Give the position of every Plasmodium parasite visible.
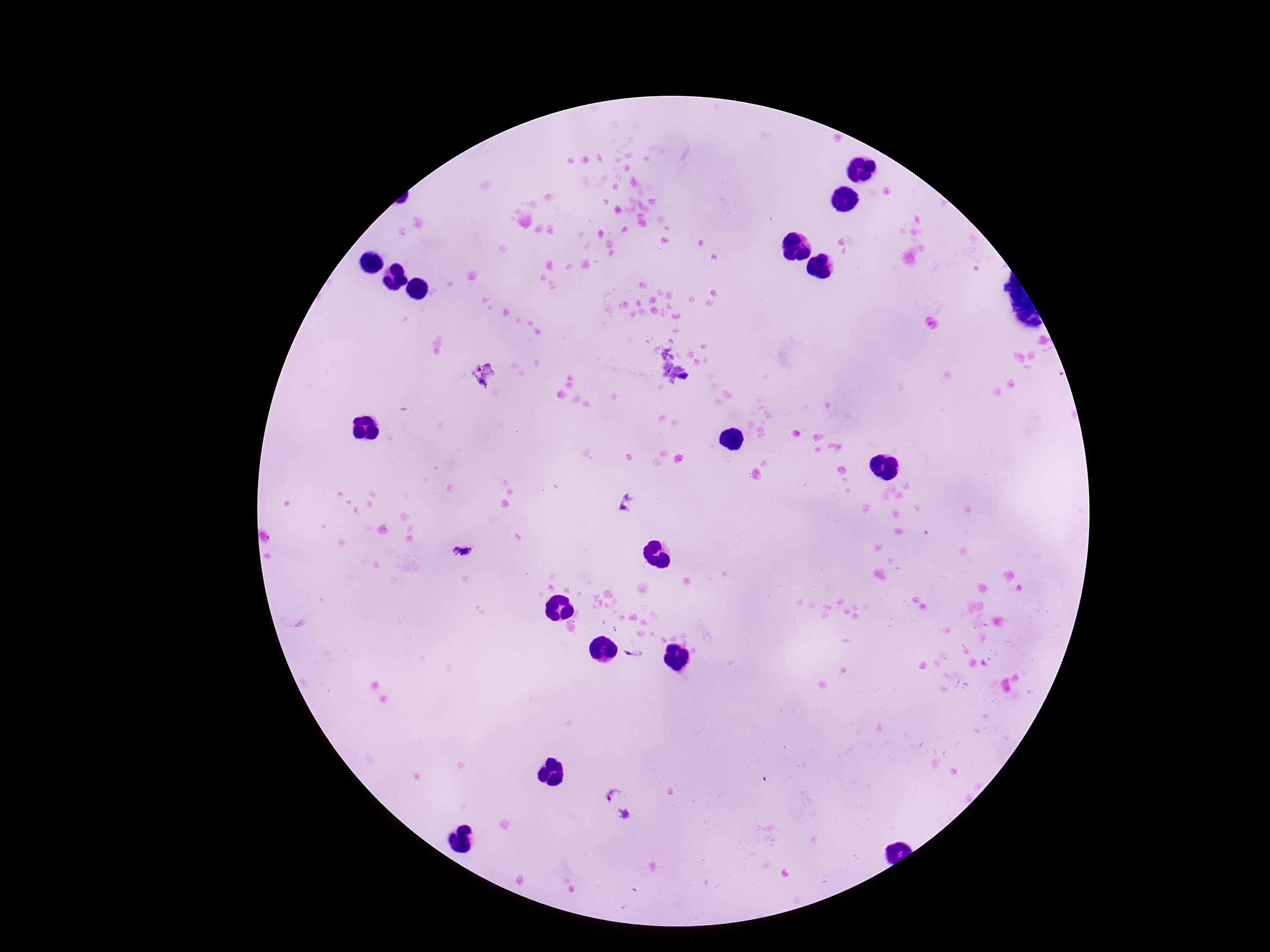

Approximate centers as (x, y) in pixels.
Plasmodium parasites: (485, 374), (626, 503), (464, 552), (615, 631), (633, 654), (619, 804).

capture = smartphone camera through the microscope eyepiece
stain = Giemsa
preparation = thick blood film
field of view = single
patient malaria status = infected
image size = 1270×952 pixels
magnification = 100x